Identify the parasite.
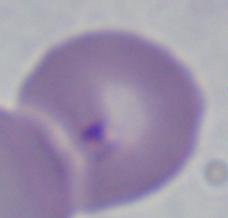

Babesia.

Summary:
  - Magnification: 1000x
  - Modality: photomicrograph